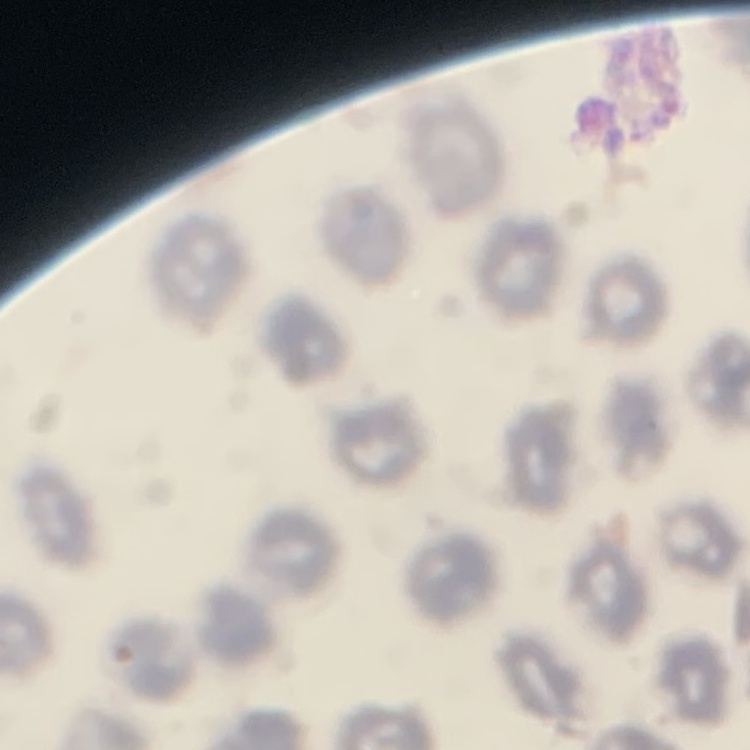

Summary:
  - Red blood cell morphology: no rouleaux formation
  - Image type: square crop of a larger photomicrograph
  - Stain: Field's or Giemsa
  - Preparation: thin blood film